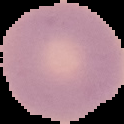
Summary:
  - Image type: segmented cell region on a black background
  - Preparation: thin blood film
  - Result: no malaria parasites detected
  - Image size: 124×124 pixels